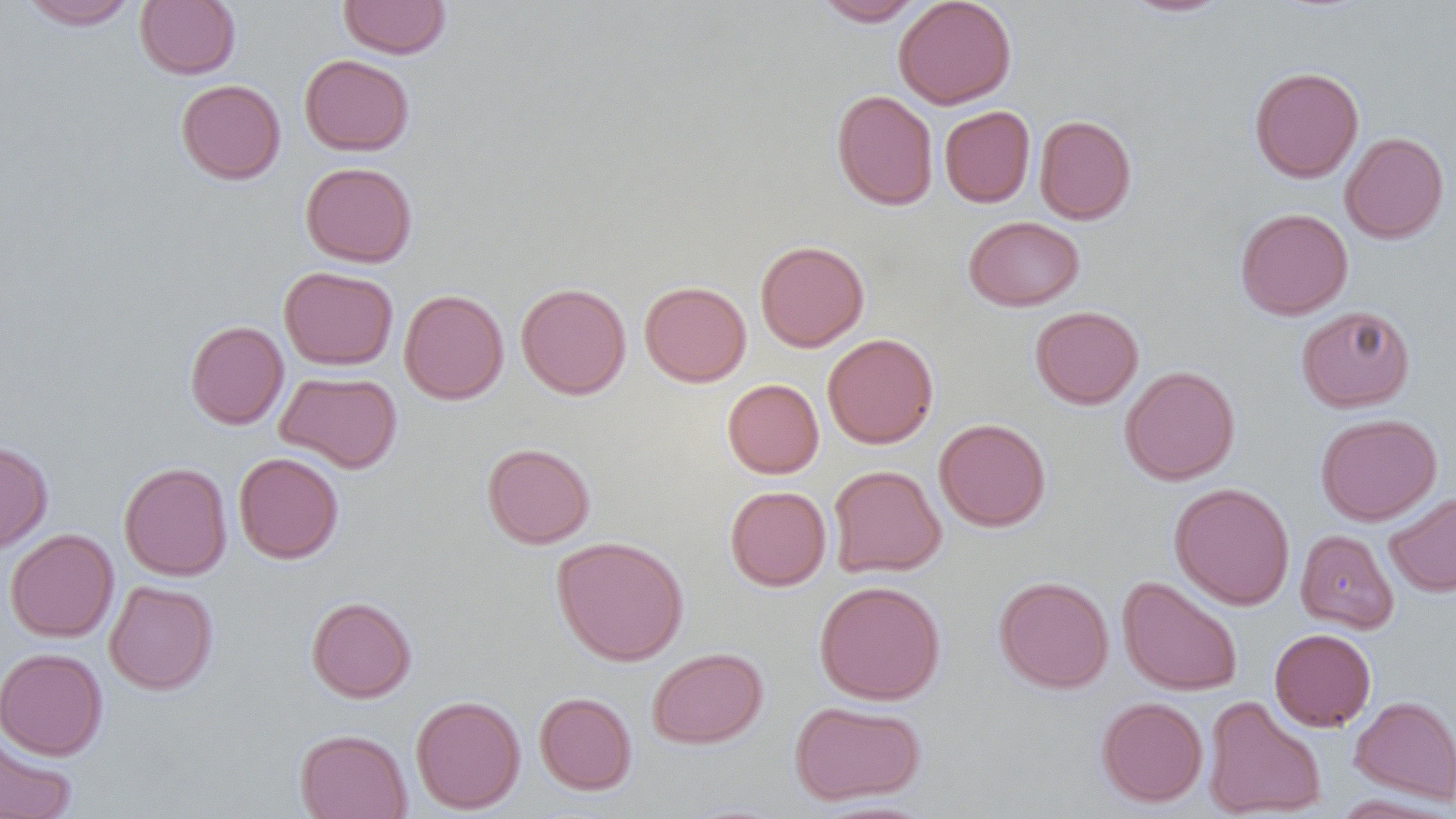

Summary:
  - Coordinate format: approximate bounding boxes as named x1/y1/x2/y2 corners in pixels
  - Uninfected red blood cell locations: (x1=17, y1=0, x2=140, y2=30), (x1=338, y1=0, x2=451, y2=59), (x1=893, y1=0, x2=1017, y2=109), (x1=1119, y1=0, x2=1234, y2=18), (x1=135, y1=1, x2=241, y2=79), (x1=815, y1=1, x2=925, y2=25), (x1=299, y1=54, x2=415, y2=156), (x1=1249, y1=66, x2=1364, y2=183), (x1=176, y1=79, x2=286, y2=184), (x1=831, y1=89, x2=939, y2=210), (x1=939, y1=105, x2=1035, y2=208), (x1=1034, y1=114, x2=1137, y2=225), (x1=1339, y1=131, x2=1449, y2=244), (x1=300, y1=162, x2=417, y2=267), (x1=1235, y1=208, x2=1353, y2=320), (x1=963, y1=215, x2=1085, y2=311), (x1=755, y1=240, x2=870, y2=352), (x1=279, y1=266, x2=398, y2=370), (x1=639, y1=280, x2=752, y2=387), (x1=515, y1=282, x2=631, y2=399), (x1=399, y1=289, x2=509, y2=404), (x1=1296, y1=305, x2=1415, y2=412), (x1=1030, y1=306, x2=1144, y2=409), (x1=184, y1=320, x2=289, y2=429), (x1=822, y1=333, x2=939, y2=448), (x1=1119, y1=365, x2=1240, y2=485), (x1=275, y1=370, x2=403, y2=474), (x1=722, y1=378, x2=824, y2=478), (x1=1315, y1=413, x2=1442, y2=526), (x1=934, y1=418, x2=1051, y2=532), (x1=0, y1=439, x2=53, y2=554), (x1=482, y1=442, x2=595, y2=549), (x1=233, y1=452, x2=344, y2=564), (x1=118, y1=462, x2=232, y2=581), (x1=828, y1=464, x2=946, y2=578), (x1=1169, y1=482, x2=1295, y2=610), (x1=724, y1=485, x2=831, y2=591), (x1=1384, y1=492, x2=1456, y2=598), (x1=5, y1=529, x2=119, y2=643), (x1=1295, y1=529, x2=1398, y2=634), (x1=552, y1=535, x2=689, y2=666), (x1=994, y1=576, x2=1114, y2=693), (x1=1118, y1=576, x2=1243, y2=696), (x1=104, y1=580, x2=218, y2=695), (x1=814, y1=580, x2=946, y2=705), (x1=306, y1=597, x2=417, y2=703), (x1=1269, y1=628, x2=1376, y2=731), (x1=0, y1=647, x2=108, y2=760), (x1=647, y1=647, x2=767, y2=749), (x1=534, y1=692, x2=637, y2=795), (x1=1350, y1=694, x2=1456, y2=805), (x1=411, y1=695, x2=526, y2=814), (x1=1202, y1=695, x2=1326, y2=818), (x1=1096, y1=696, x2=1208, y2=807), (x1=789, y1=700, x2=926, y2=805), (x1=294, y1=729, x2=412, y2=819), (x1=0, y1=733, x2=77, y2=819), (x1=1329, y1=793, x2=1455, y2=818), (x1=809, y1=799, x2=938, y2=819)
  - Slide-level diagnosis: negative for blood parasites
  - Magnification: 1000x
  - Preparation: thin blood film
  - Field of view: one of a larger specimen
  - Modality: optical microscopy
  - Image size: 1456×819 pixels